Classify this cell by malaria status.
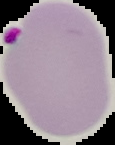
It is uninfected.

Image is 115×145 pixels. From a thin blood film. Cell region segmented out of the field of view; the surrounding area is masked to black.